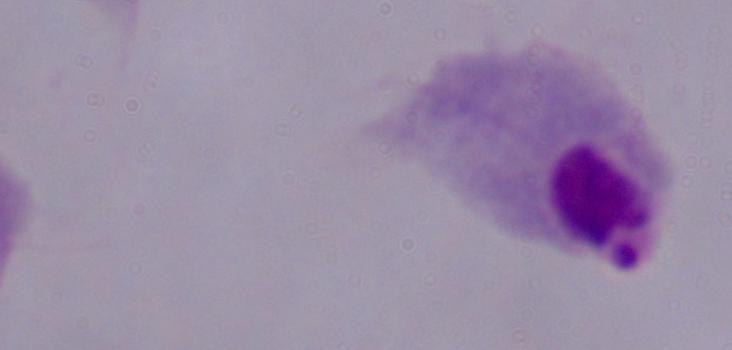

Summary:
  - Magnification: 1000x
  - Identification: trichomonad
  - Modality: photomicrograph